Identify the parasite.
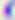

This is Toxoplasma gondii.

Photomicrograph. 400x magnification.